Outline each blood parasite and name the species.
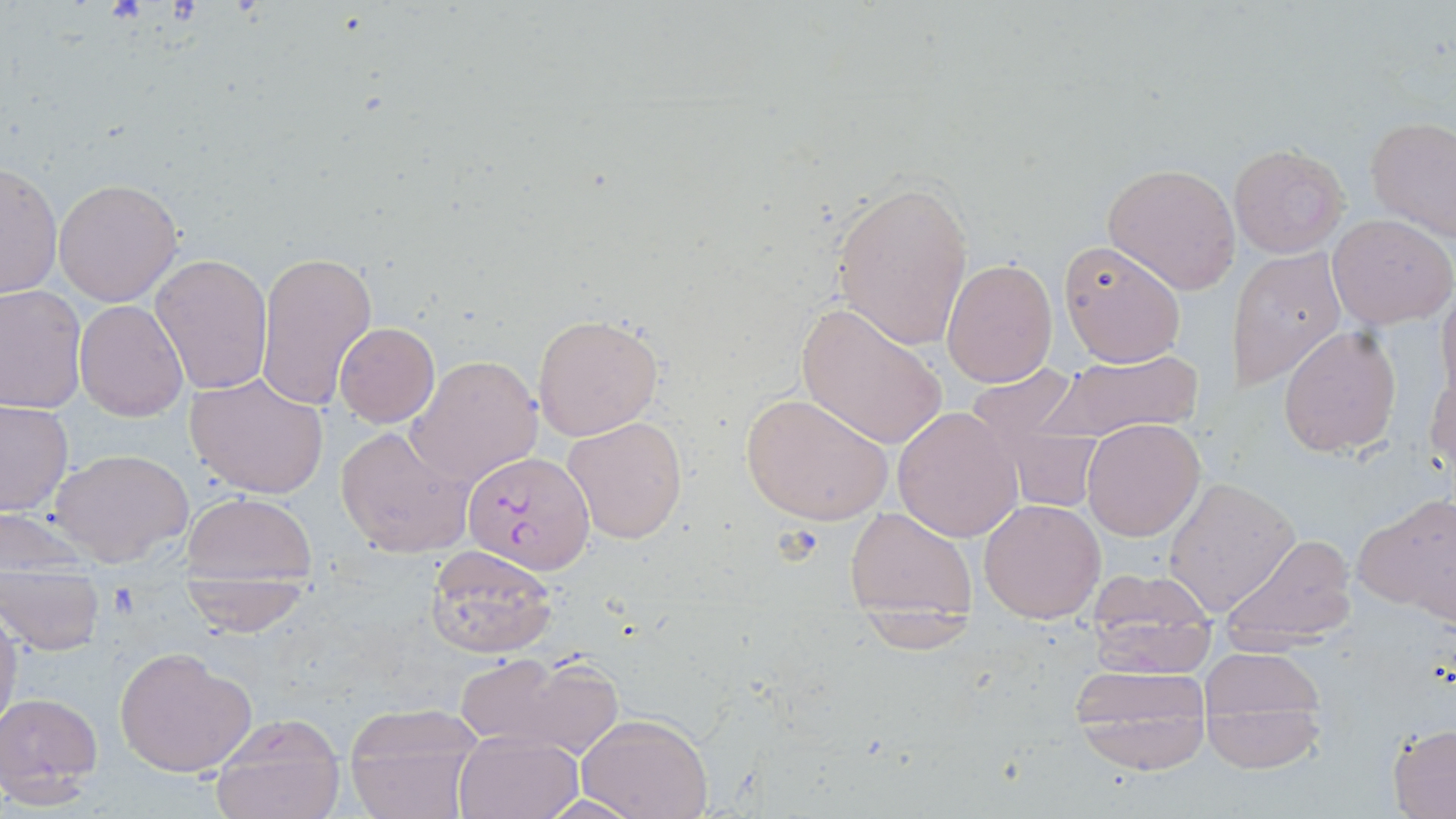
Approximate bounding boxes as (x1,y1)-(x2,y2) corner pairs in pixels.
Plasmodium falciparum-infected red blood cells: (462,450)-(593,572).
No Plasmodium ovale, Plasmodium malariae, Plasmodium vivax, Babesia divergens, or Trypanosoma brucei observed.

Summary:
  - Uninfected red blood cell locations: (1365,114)-(1456,242), (1230,142)-(1348,258), (1,162)-(63,301), (1102,163)-(1241,294), (828,176)-(974,351), (53,179)-(182,304), (1328,212)-(1454,328), (1059,243)-(1186,367), (1230,247)-(1345,387), (254,250)-(377,411), (150,253)-(273,395), (940,257)-(1057,389), (0,287)-(87,411), (1436,287)-(1456,411), (75,300)-(188,420), (794,303)-(948,451), (534,314)-(663,439), (334,322)-(439,426), (1279,326)-(1401,456), (1045,346)-(1204,443), (406,355)-(543,486), (962,364)-(1096,490), (1426,366)-(1456,483), (186,371)-(330,499), (740,390)-(893,526), (0,400)-(74,517), (891,404)-(1022,541), (564,416)-(687,543), (1082,419)-(1205,540), (335,423)-(474,559), (49,447)-(192,566), (1163,476)-(1300,616), (182,492)-(315,582), (1358,494)-(1456,622), (978,498)-(1106,623), (845,508)-(976,621), (1,509)-(94,575), (1219,531)-(1358,646), (424,543)-(561,660), (1083,566)-(1219,674), (1,569)-(105,655), (177,575)-(310,635), (0,606)-(21,740), (1196,644)-(1329,753), (113,646)-(257,778), (455,651)-(616,756), (1064,664)-(1214,751), (1,691)-(103,799), (345,707)-(485,817), (576,712)-(714,819), (209,715)-(347,819), (1388,725)-(1456,815), (455,730)-(583,819)
  - Slide-level diagnosis: Plasmodium falciparum
  - Stain: May-Grünwald-Giemsa
  - Image size: 1456×819 pixels
  - Preparation: thin blood film
  - Magnification: 1000x
  - Modality: optical microscopy
  - Field of view: single